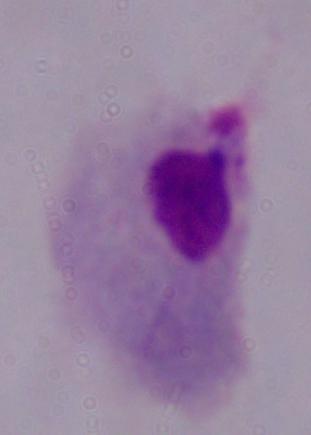
modality: photomicrograph
identification: trichomonad
magnification: 1000x